Assess this cell for malaria.
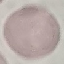
It is uninfected.

capture = smartphone through the microscope eyepiece
preparation = thin blood smear
stain = Giemsa
image type = automatically extracted cell patch, resized to 64 × 64 pixels